Give the extent of all uninfected red blood cells.
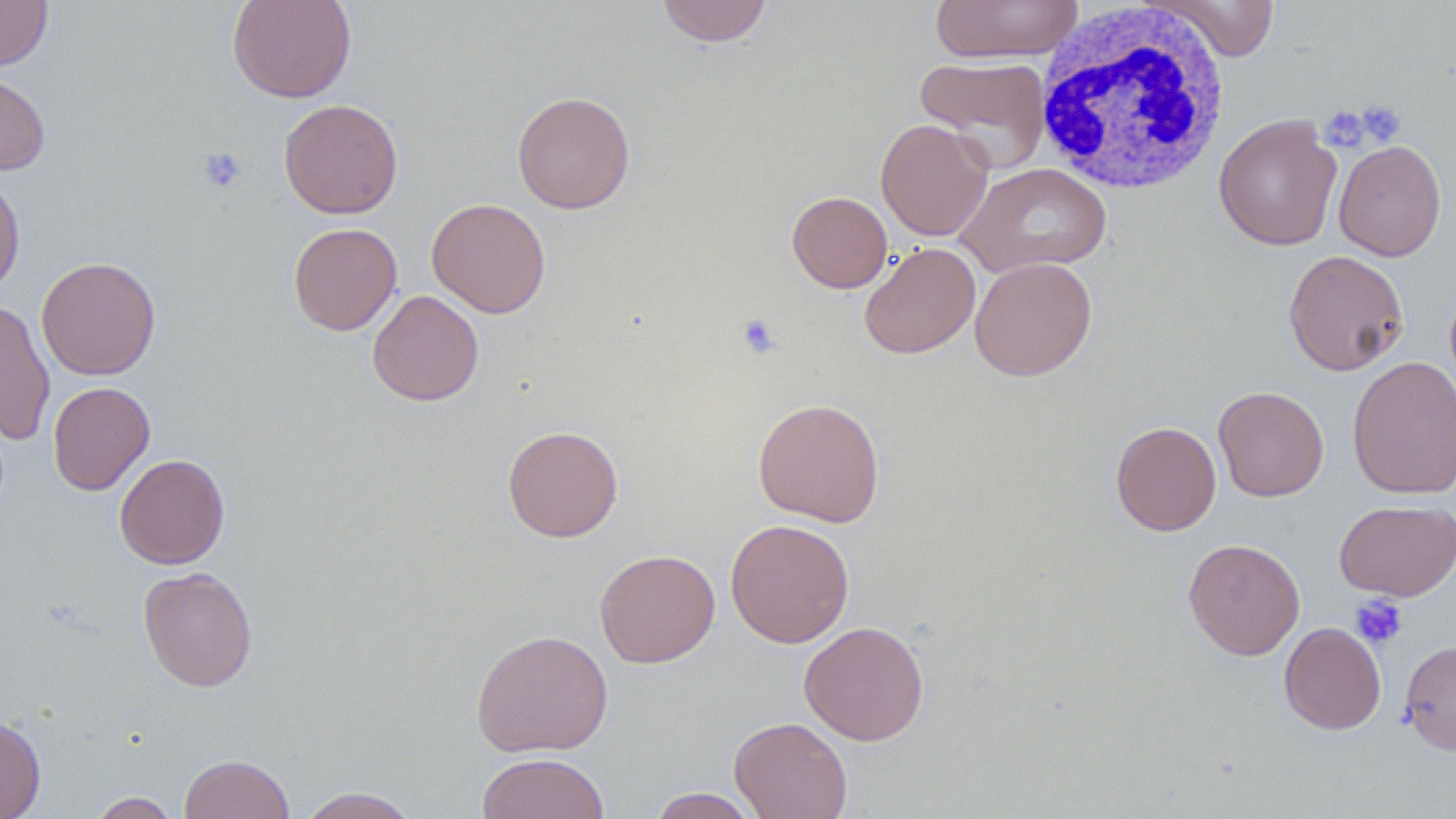
Approximate bounding boxes as [x1, y1, x2, y2] in pixels.
Uninfected red blood cells: [0, 0, 53, 72], [227, 0, 357, 103], [930, 0, 1083, 65], [1145, 0, 1282, 61], [655, 1, 774, 47], [915, 55, 1051, 172], [0, 71, 51, 176], [512, 91, 636, 214], [278, 99, 403, 219], [1213, 113, 1342, 251], [876, 119, 994, 241], [1333, 139, 1447, 262], [956, 163, 1113, 279], [0, 172, 25, 298], [787, 190, 893, 293], [426, 197, 551, 318], [287, 222, 402, 335], [859, 242, 981, 359], [1283, 250, 1408, 375], [36, 257, 161, 380], [969, 257, 1097, 381], [367, 289, 484, 406], [0, 300, 56, 445], [1347, 355, 1456, 500], [47, 381, 155, 495], [1213, 385, 1329, 501], [752, 397, 886, 527], [1110, 421, 1221, 536], [502, 425, 623, 542], [114, 453, 230, 569], [1335, 499, 1456, 601], [725, 518, 855, 648], [1183, 539, 1305, 660], [594, 549, 720, 668], [138, 566, 258, 692], [798, 621, 930, 745], [1279, 622, 1386, 734], [471, 628, 613, 758], [1400, 639, 1456, 755], [0, 715, 46, 819], [729, 716, 852, 819], [477, 752, 611, 818], [178, 753, 295, 819], [297, 787, 422, 818], [647, 788, 764, 818], [87, 792, 181, 819].

slide_level_diagnosis: negative for blood parasites
field_of_view: one of a larger specimen
image_size: 1456×819 pixels
white_blood_cell_locations: 'approximate bounding boxes as [x1, y1, x2, y2] in pixels: [1032, 2, 1232, 196]'
preparation: thin blood film
magnification: 1000x
platelet_locations: 'approximate bounding boxes as [x1, y1, x2, y2] in pixels: [1356, 99, 1407, 146], [1320, 106, 1370, 152], [197, 147, 247, 193], [736, 313, 783, 360], [1350, 594, 1408, 649]'
modality: light microscopy
stain: May-Grünwald-Giemsa